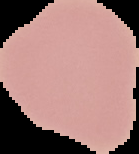

Summary:
  - Image type: cell region segmented out of the field of view; surrounding area masked to black
  - Image size: 139×154 pixels
  - Result: no Plasmodium parasites seen
  - Preparation: thin blood film